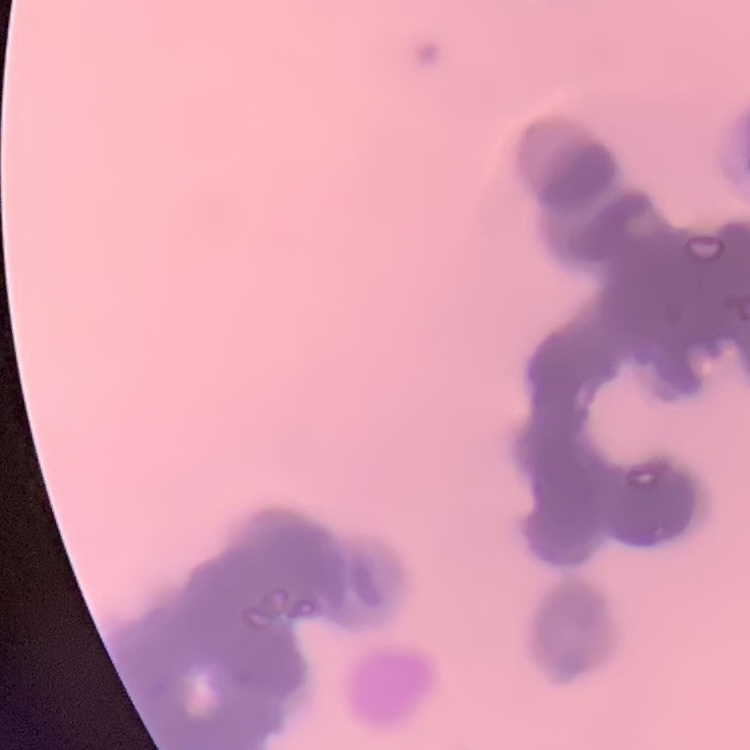

The red blood cells show rouleaux formation. One tile cut from a larger photomicrograph. Thin blood film. Field's or Giemsa stain.